Report the malaria status of this cell.
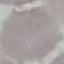

It is uninfected.

Acquired by smartphone through the microscope eyepiece. Giemsa stain. Automatically extracted cell patch, resized to 64 × 64 pixels. Thin blood film.